Classify this cell by malaria status.
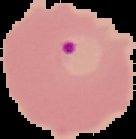
Parasitized.

{
  "image_size": "136×139 pixels",
  "preparation": "thin blood film",
  "image_type": "segmented cell region with the area outside set to black"
}